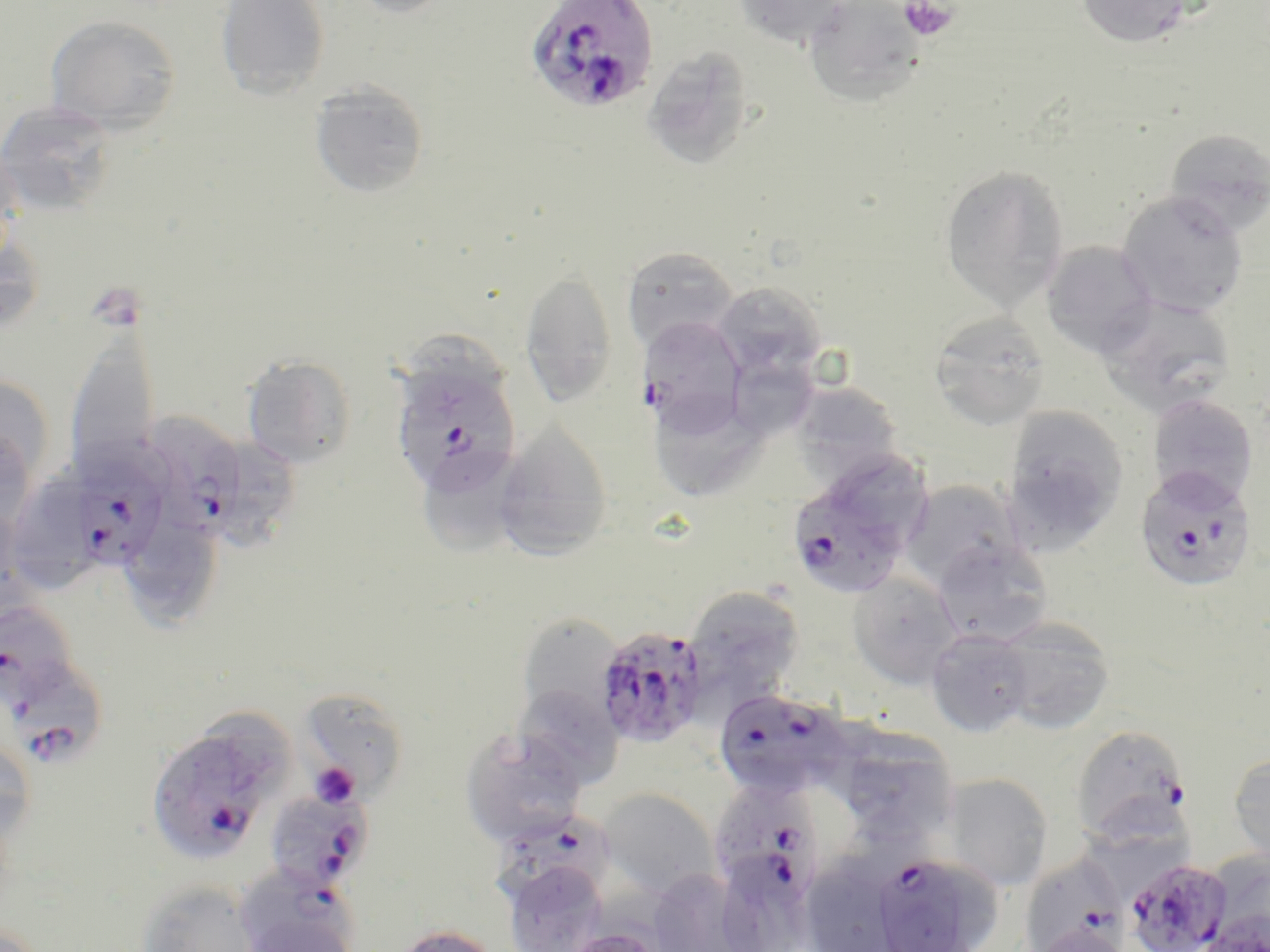 Approximate bounding boxes as named x1/y1/x2/y2 corners in pixels. Plasmodium falciparum-infected red blood cell locations: (x1=525, y1=0, x2=659, y2=114), (x1=638, y1=315, x2=747, y2=432), (x1=390, y1=353, x2=523, y2=496), (x1=143, y1=413, x2=242, y2=536), (x1=72, y1=457, x2=168, y2=570), (x1=783, y1=457, x2=926, y2=602), (x1=1134, y1=465, x2=1257, y2=593), (x1=593, y1=624, x2=710, y2=748), (x1=16, y1=665, x2=106, y2=773), (x1=714, y1=693, x2=852, y2=805), (x1=145, y1=719, x2=287, y2=867), (x1=1070, y1=724, x2=1193, y2=843), (x1=719, y1=785, x2=825, y2=908), (x1=264, y1=788, x2=375, y2=892), (x1=490, y1=814, x2=616, y2=911), (x1=869, y1=852, x2=998, y2=952), (x1=1018, y1=854, x2=1129, y2=952), (x1=1124, y1=858, x2=1233, y2=952), (x1=235, y1=881, x2=362, y2=952). Platelet locations: (x1=899, y1=1, x2=958, y2=42), (x1=309, y1=762, x2=361, y2=808). Uninfected red blood cell locations: (x1=216, y1=0, x2=330, y2=101), (x1=341, y1=0, x2=459, y2=19), (x1=732, y1=0, x2=850, y2=49), (x1=801, y1=0, x2=927, y2=109), (x1=1075, y1=0, x2=1196, y2=48), (x1=44, y1=15, x2=182, y2=133), (x1=641, y1=45, x2=754, y2=170), (x1=309, y1=79, x2=429, y2=199), (x1=0, y1=100, x2=118, y2=217), (x1=1164, y1=129, x2=1270, y2=236), (x1=0, y1=135, x2=24, y2=268), (x1=939, y1=164, x2=1070, y2=313), (x1=1116, y1=190, x2=1250, y2=317), (x1=1040, y1=241, x2=1158, y2=358), (x1=621, y1=246, x2=738, y2=354), (x1=519, y1=266, x2=618, y2=409), (x1=712, y1=282, x2=828, y2=386), (x1=1096, y1=294, x2=1236, y2=418), (x1=929, y1=311, x2=1051, y2=431), (x1=64, y1=328, x2=160, y2=483), (x1=734, y1=353, x2=821, y2=448), (x1=242, y1=354, x2=357, y2=469), (x1=0, y1=375, x2=56, y2=488), (x1=789, y1=381, x2=904, y2=488), (x1=1146, y1=393, x2=1259, y2=508), (x1=658, y1=396, x2=767, y2=498), (x1=1001, y1=406, x2=1129, y2=550), (x1=493, y1=425, x2=613, y2=563), (x1=0, y1=430, x2=36, y2=533), (x1=225, y1=436, x2=304, y2=555), (x1=426, y1=456, x2=535, y2=556), (x1=13, y1=471, x2=83, y2=595), (x1=899, y1=480, x2=1028, y2=593), (x1=129, y1=516, x2=224, y2=620), (x1=931, y1=536, x2=1053, y2=645), (x1=847, y1=571, x2=964, y2=688), (x1=683, y1=585, x2=805, y2=705), (x1=1, y1=603, x2=80, y2=705), (x1=517, y1=613, x2=625, y2=722), (x1=993, y1=616, x2=1116, y2=734), (x1=925, y1=628, x2=1034, y2=736), (x1=514, y1=684, x2=623, y2=788), (x1=297, y1=687, x2=411, y2=801), (x1=459, y1=726, x2=587, y2=848), (x1=851, y1=729, x2=956, y2=851), (x1=0, y1=739, x2=36, y2=861), (x1=1228, y1=750, x2=1270, y2=866), (x1=940, y1=772, x2=1054, y2=891), (x1=598, y1=787, x2=719, y2=899), (x1=814, y1=847, x2=899, y2=952), (x1=1204, y1=850, x2=1270, y2=949), (x1=727, y1=858, x2=816, y2=952), (x1=503, y1=859, x2=609, y2=951), (x1=647, y1=867, x2=752, y2=951), (x1=135, y1=881, x2=263, y2=952), (x1=389, y1=924, x2=502, y2=952), (x1=561, y1=926, x2=665, y2=952). Slide-level diagnosis: Plasmodium falciparum. May-Grünwald-Giemsa-stained preparation. Single field of view. Captured at 1000x magnification. Thin blood smear. Image is 1270×952 pixels. Light microscopy.